State which parasite is depicted.
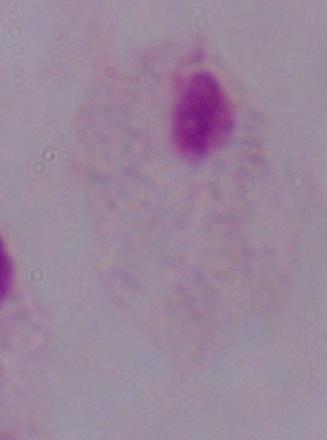
A trichomonad.

1000x magnification. Micrograph.